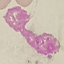
Summary:
  - Result: negative for malaria parasites
  - Preparation: thin blood film
  - Image type: automatically extracted cell patch, resized to 64 × 64 pixels
  - Stain: Giemsa
  - Capture: smartphone through the microscope eyepiece